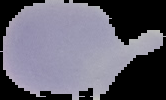
image size = 166×100 pixels
result = no malaria parasites detected
preparation = thin blood smear
image type = cell region segmented out of the field of view; surrounding area masked to black